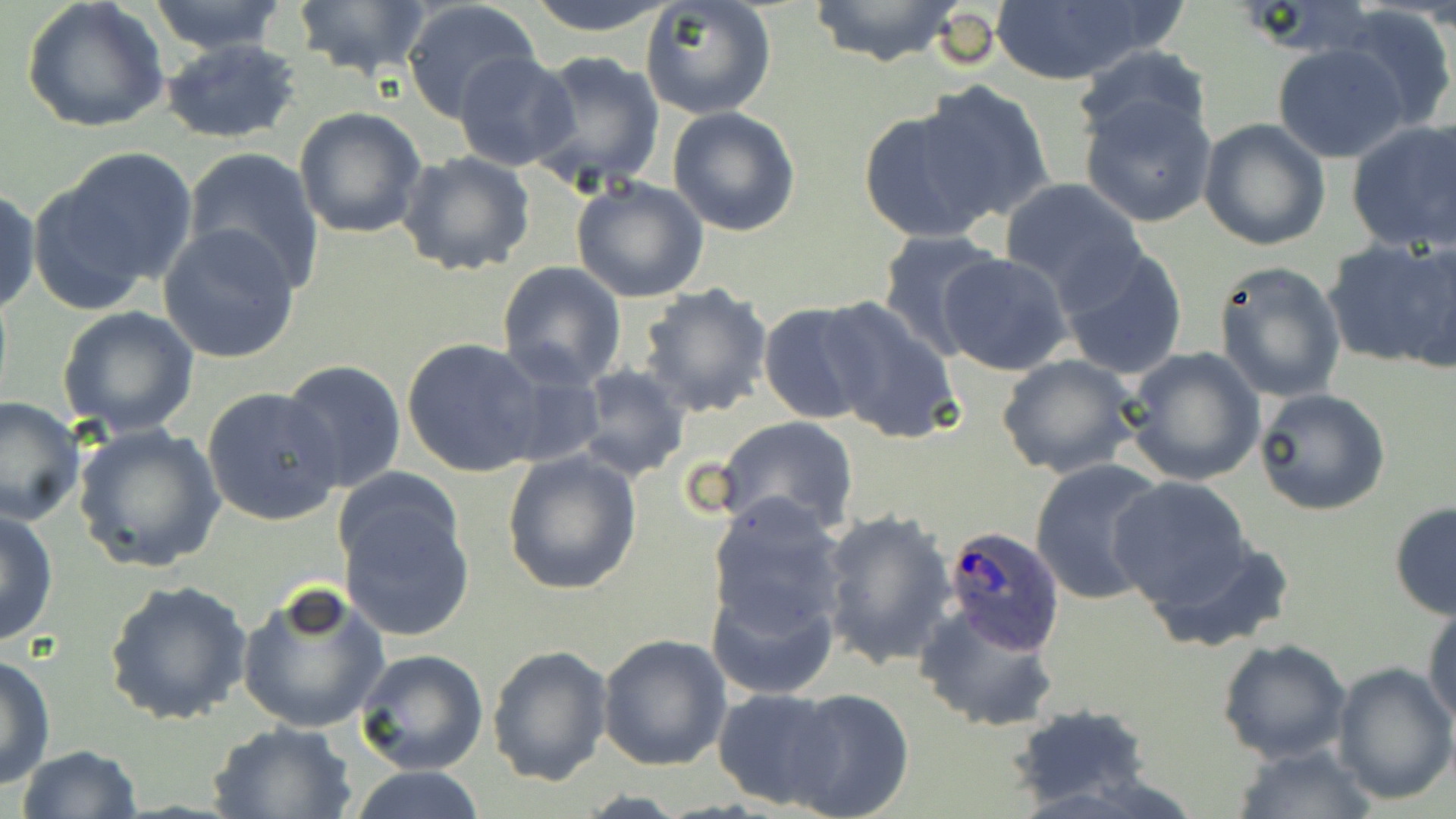

slide-level diagnosis = Plasmodium ovale
magnification = 1000x
stain = May-Grünwald-Giemsa
uninfected red blood cell locations = approximate bounding boxes as named x1/y1/x2/y2 corners in pixels: (x1=21, y1=0, x2=170, y2=136), (x1=288, y1=0, x2=436, y2=82), (x1=399, y1=0, x2=542, y2=123), (x1=523, y1=0, x2=680, y2=37), (x1=806, y1=0, x2=965, y2=68), (x1=987, y1=0, x2=1177, y2=87), (x1=146, y1=1, x2=290, y2=55), (x1=642, y1=1, x2=777, y2=120), (x1=1335, y1=8, x2=1453, y2=133), (x1=161, y1=38, x2=304, y2=146), (x1=1272, y1=42, x2=1409, y2=163), (x1=1072, y1=45, x2=1210, y2=147), (x1=453, y1=51, x2=583, y2=172), (x1=528, y1=52, x2=666, y2=191), (x1=915, y1=82, x2=1055, y2=221), (x1=1077, y1=91, x2=1221, y2=229), (x1=293, y1=106, x2=428, y2=239), (x1=667, y1=106, x2=801, y2=236), (x1=857, y1=106, x2=1000, y2=244), (x1=1198, y1=118, x2=1332, y2=251), (x1=1346, y1=119, x2=1456, y2=253), (x1=33, y1=146, x2=199, y2=306), (x1=182, y1=147, x2=325, y2=294), (x1=396, y1=151, x2=536, y2=278), (x1=570, y1=177, x2=712, y2=302), (x1=1000, y1=179, x2=1145, y2=304), (x1=0, y1=188, x2=41, y2=317), (x1=159, y1=225, x2=302, y2=364), (x1=875, y1=229, x2=1008, y2=360), (x1=1325, y1=236, x2=1452, y2=370), (x1=1398, y1=238, x2=1456, y2=375), (x1=1056, y1=246, x2=1190, y2=381), (x1=936, y1=253, x2=1074, y2=376), (x1=1212, y1=260, x2=1348, y2=403), (x1=497, y1=261, x2=627, y2=389), (x1=638, y1=282, x2=774, y2=417), (x1=818, y1=296, x2=963, y2=446), (x1=756, y1=302, x2=880, y2=424), (x1=56, y1=306, x2=200, y2=436), (x1=401, y1=337, x2=548, y2=477), (x1=1120, y1=347, x2=1265, y2=487), (x1=996, y1=354, x2=1142, y2=479), (x1=281, y1=359, x2=407, y2=494), (x1=576, y1=365, x2=690, y2=480), (x1=202, y1=387, x2=343, y2=526), (x1=1254, y1=387, x2=1390, y2=515), (x1=1, y1=396, x2=84, y2=527), (x1=712, y1=415, x2=860, y2=538), (x1=72, y1=421, x2=227, y2=572), (x1=501, y1=451, x2=643, y2=596), (x1=1029, y1=456, x2=1169, y2=607), (x1=1109, y1=477, x2=1259, y2=609), (x1=335, y1=488, x2=475, y2=643), (x1=703, y1=494, x2=849, y2=643), (x1=1388, y1=502, x2=1456, y2=621), (x1=0, y1=507, x2=59, y2=648), (x1=818, y1=507, x2=958, y2=670), (x1=1136, y1=531, x2=1299, y2=657), (x1=707, y1=579, x2=838, y2=701), (x1=105, y1=580, x2=250, y2=726), (x1=235, y1=583, x2=391, y2=736), (x1=913, y1=600, x2=1062, y2=734), (x1=1424, y1=603, x2=1456, y2=730), (x1=598, y1=635, x2=732, y2=773), (x1=1217, y1=636, x2=1352, y2=764), (x1=486, y1=643, x2=615, y2=787), (x1=355, y1=649, x2=489, y2=775), (x1=0, y1=652, x2=56, y2=792), (x1=1330, y1=661, x2=1456, y2=803), (x1=714, y1=688, x2=844, y2=808), (x1=783, y1=690, x2=914, y2=819), (x1=1008, y1=705, x2=1153, y2=811), (x1=206, y1=720, x2=357, y2=818), (x1=1230, y1=743, x2=1378, y2=819), (x1=14, y1=744, x2=145, y2=819), (x1=345, y1=764, x2=491, y2=819)
modality = optical microscopy
Plasmodium ovale-infected red blood cell locations = approximate bounding boxes as named x1/y1/x2/y2 corners in pixels: (x1=940, y1=526, x2=1064, y2=654)
preparation = thin blood film
image size = 1456×819 pixels
field of view = one of a larger specimen